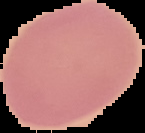
Summary:
  - Preparation: thin blood smear
  - Image type: segmented cell region on a black background
  - Malaria status: uninfected
  - Image size: 145×133 pixels